Identify the parasite.
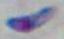
This is Toxoplasma gondii.

Summary:
  - Modality: photomicrograph
  - Magnification: 1000x